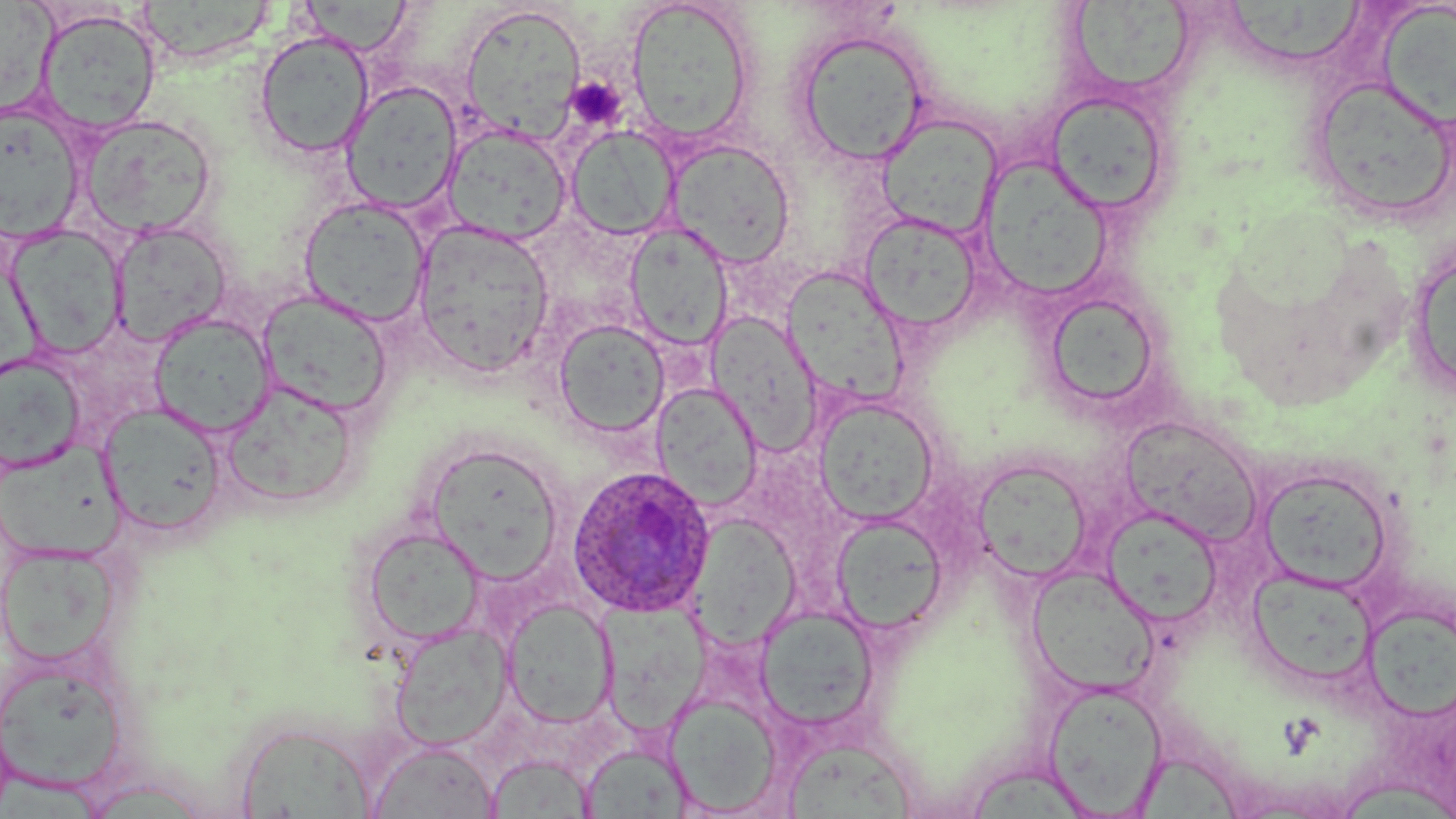
plasmodium_ovale_infected_red_blood_cell_locations: 'approximate bounding boxes as named x1/y1/x2/y2 corners in pixels: (x1=565, y1=465, x2=717, y2=618)'
slide_level_diagnosis: Plasmodium ovale
preparation: thin blood smear
modality: optical microscopy
field_of_view: single
image_size: 1456×819 pixels
platelet_locations: 'approximate bounding boxes as named x1/y1/x2/y2 corners in pixels: (x1=564, y1=77, x2=627, y2=131)'
stain: May-Grünwald-Giemsa
magnification: 1000x
uninfected_red_blood_cell_locations: 'approximate bounding boxes as named x1/y1/x2/y2 corners in pixels: (x1=0, y1=0, x2=64, y2=123), (x1=1067, y1=0, x2=1199, y2=94), (x1=300, y1=1, x2=412, y2=55), (x1=625, y1=1, x2=756, y2=146), (x1=1228, y1=2, x2=1369, y2=62), (x1=138, y1=3, x2=272, y2=62), (x1=460, y1=4, x2=587, y2=144), (x1=1379, y1=4, x2=1456, y2=130), (x1=36, y1=9, x2=161, y2=135), (x1=792, y1=27, x2=930, y2=166), (x1=254, y1=31, x2=374, y2=159), (x1=1308, y1=76, x2=1455, y2=223), (x1=341, y1=80, x2=463, y2=216), (x1=1045, y1=90, x2=1171, y2=216), (x1=1, y1=103, x2=86, y2=242), (x1=876, y1=113, x2=1003, y2=239), (x1=81, y1=114, x2=216, y2=240), (x1=443, y1=123, x2=571, y2=245), (x1=566, y1=124, x2=680, y2=240), (x1=666, y1=138, x2=796, y2=268), (x1=977, y1=155, x2=1116, y2=301), (x1=299, y1=196, x2=431, y2=327), (x1=858, y1=213, x2=982, y2=334), (x1=412, y1=220, x2=555, y2=376), (x1=111, y1=221, x2=232, y2=346), (x1=625, y1=223, x2=733, y2=351), (x1=6, y1=224, x2=127, y2=359), (x1=1405, y1=241, x2=1455, y2=399), (x1=783, y1=273, x2=913, y2=407), (x1=256, y1=291, x2=393, y2=417), (x1=1043, y1=291, x2=1164, y2=413), (x1=149, y1=312, x2=276, y2=437), (x1=713, y1=316, x2=827, y2=458), (x1=553, y1=319, x2=670, y2=438), (x1=0, y1=353, x2=87, y2=473), (x1=220, y1=380, x2=361, y2=507), (x1=650, y1=381, x2=763, y2=512), (x1=813, y1=396, x2=940, y2=525), (x1=99, y1=404, x2=228, y2=537), (x1=1119, y1=416, x2=1264, y2=546), (x1=1, y1=436, x2=126, y2=562), (x1=428, y1=452, x2=558, y2=584), (x1=971, y1=458, x2=1093, y2=583), (x1=1254, y1=464, x2=1397, y2=595), (x1=1100, y1=506, x2=1224, y2=628), (x1=688, y1=510, x2=802, y2=652), (x1=830, y1=513, x2=949, y2=636), (x1=361, y1=525, x2=488, y2=647), (x1=0, y1=544, x2=122, y2=668), (x1=1025, y1=565, x2=1159, y2=698), (x1=1246, y1=567, x2=1377, y2=688), (x1=599, y1=597, x2=709, y2=738), (x1=502, y1=598, x2=618, y2=728), (x1=754, y1=605, x2=881, y2=734), (x1=1362, y1=608, x2=1456, y2=726), (x1=390, y1=623, x2=512, y2=751), (x1=0, y1=658, x2=129, y2=795), (x1=1043, y1=680, x2=1168, y2=816), (x1=665, y1=692, x2=783, y2=814), (x1=232, y1=719, x2=379, y2=818), (x1=366, y1=740, x2=499, y2=818), (x1=784, y1=743, x2=917, y2=819), (x1=580, y1=744, x2=691, y2=818), (x1=486, y1=754, x2=595, y2=818), (x1=1134, y1=755, x2=1248, y2=819), (x1=969, y1=765, x2=1082, y2=819)'